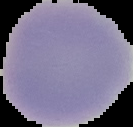

{
  "preparation": "thin blood film",
  "image_size": "133×127 pixels",
  "image_type": "cell region segmented out of the field of view; surrounding area masked to black",
  "result": "no malaria parasites seen"
}